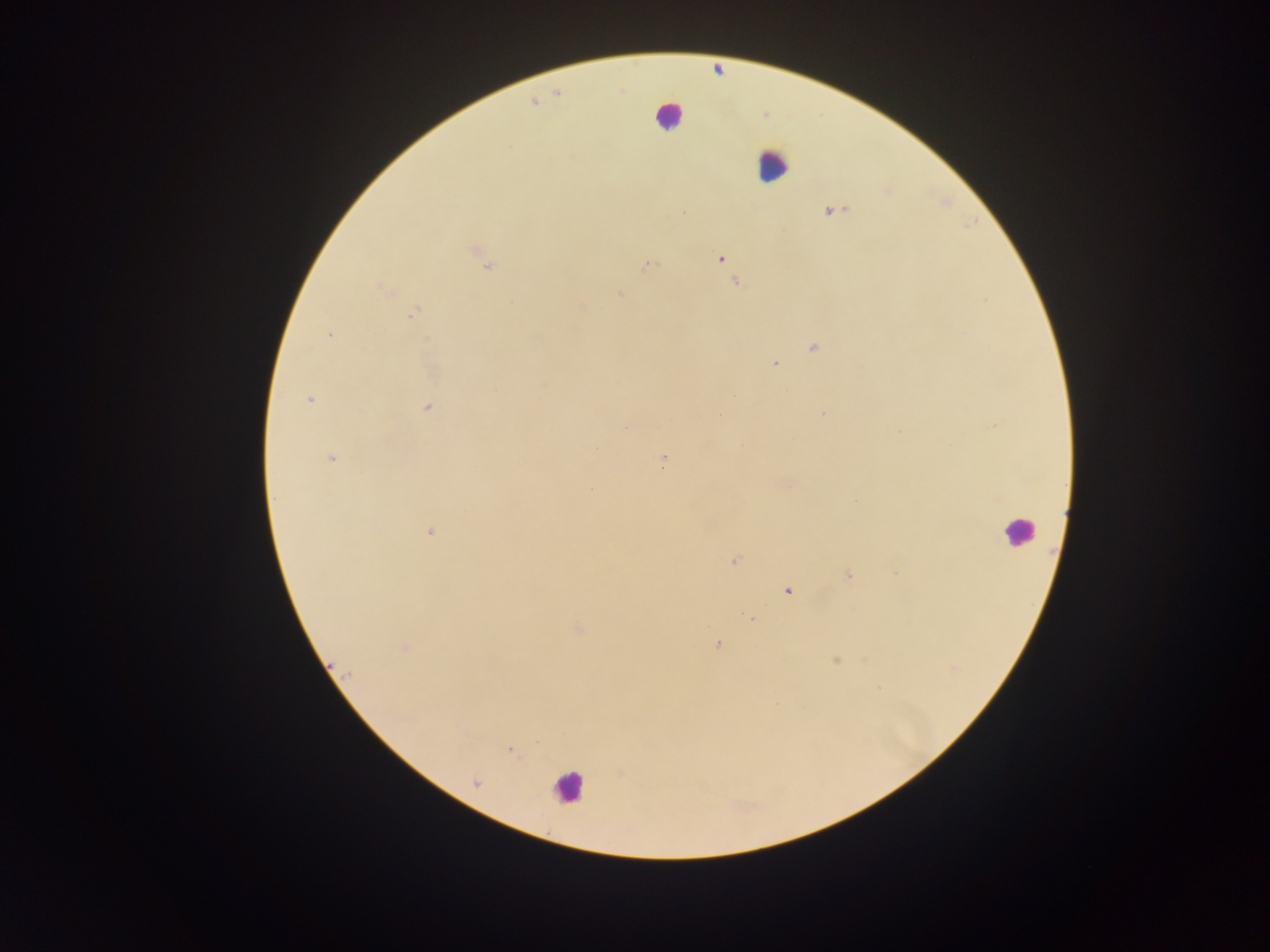
preparation = thick blood film
image size = 1270×952 pixels
leukocyte locations = approximate centers as x y in pixels: 668 116; 773 164; 1016 531; 567 788
field of view = single
capture = mobile-phone photograph through a microscope
country = Ghana
malaria parasite locations = approximate centers as x y in pixels: 832 210; 721 258; 647 264; 489 266; 736 283; 381 288; 620 294; 581 306; 412 314; 328 335; 813 348; 775 364; 733 395; 309 398; 428 407; 822 413; 719 417; 901 431; 330 458; 663 458; 787 483; 855 501; 429 532; 733 561; 897 572; 847 575; 788 591; 752 619; 578 628; 717 644; 404 648; 836 660; 954 669; 879 688; 510 749; 475 783